Assess this cell for malaria.
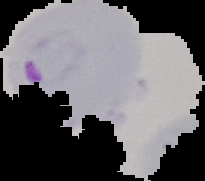

It is parasitized.

image size = 205×181 pixels
image type = cell region segmented out of the field of view; surrounding area masked to black
preparation = thin blood smear